State the preparation type.
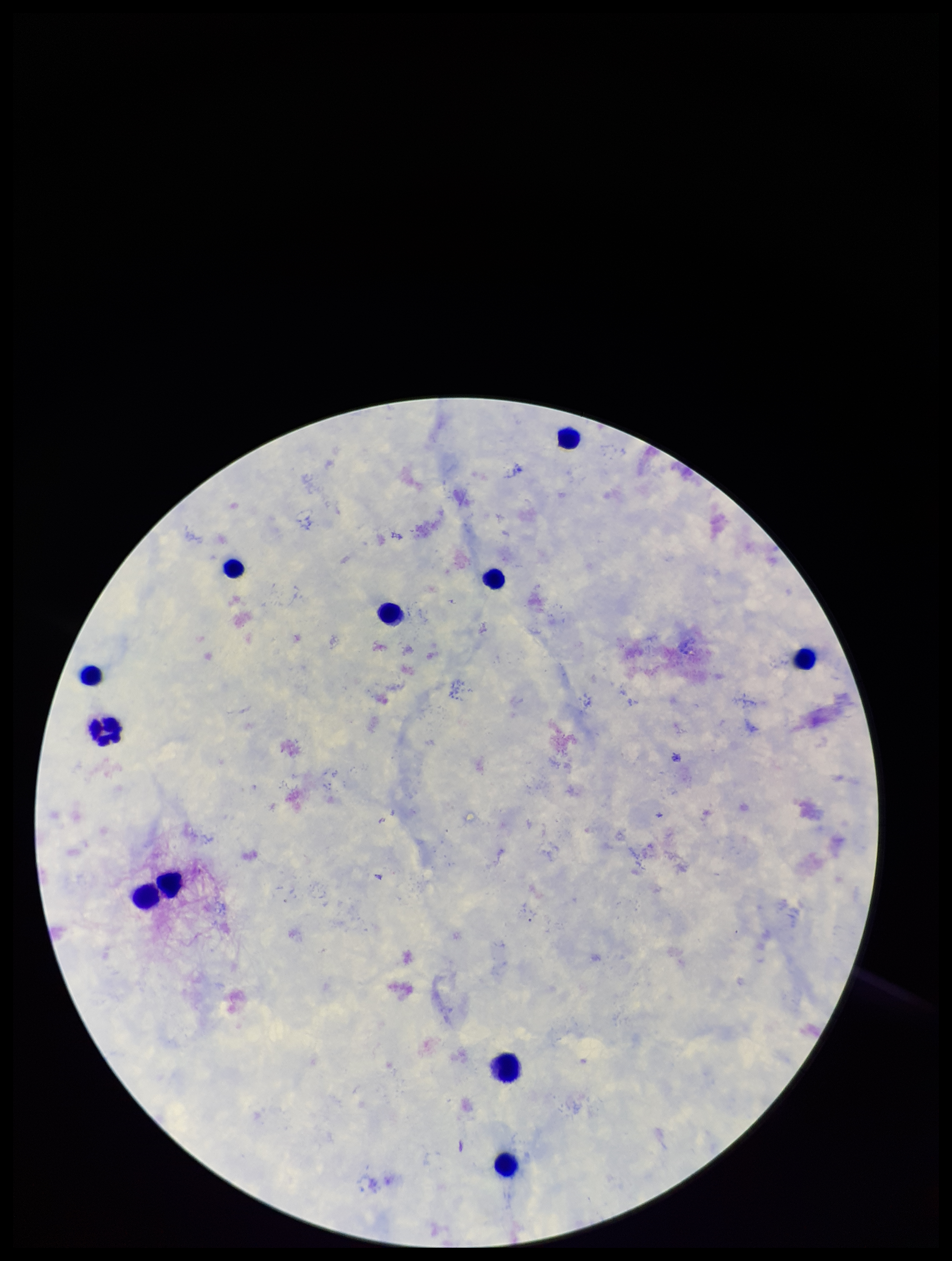
Thick.

Summary:
  - Field of view: one from this slide
  - Patient malaria status: negative
  - Image size: 952×1261 pixels
  - Stain: Giemsa
  - Capture: smartphone photograph through the microscope eyepiece
  - Parasite count: 0
  - Leukocyte count: 11
  - Plasmodium parasites: none seen